Name the parasite shown.
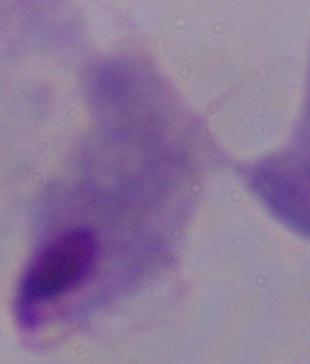
This is a trichomonad.

Micrograph. Captured at 1000x magnification.